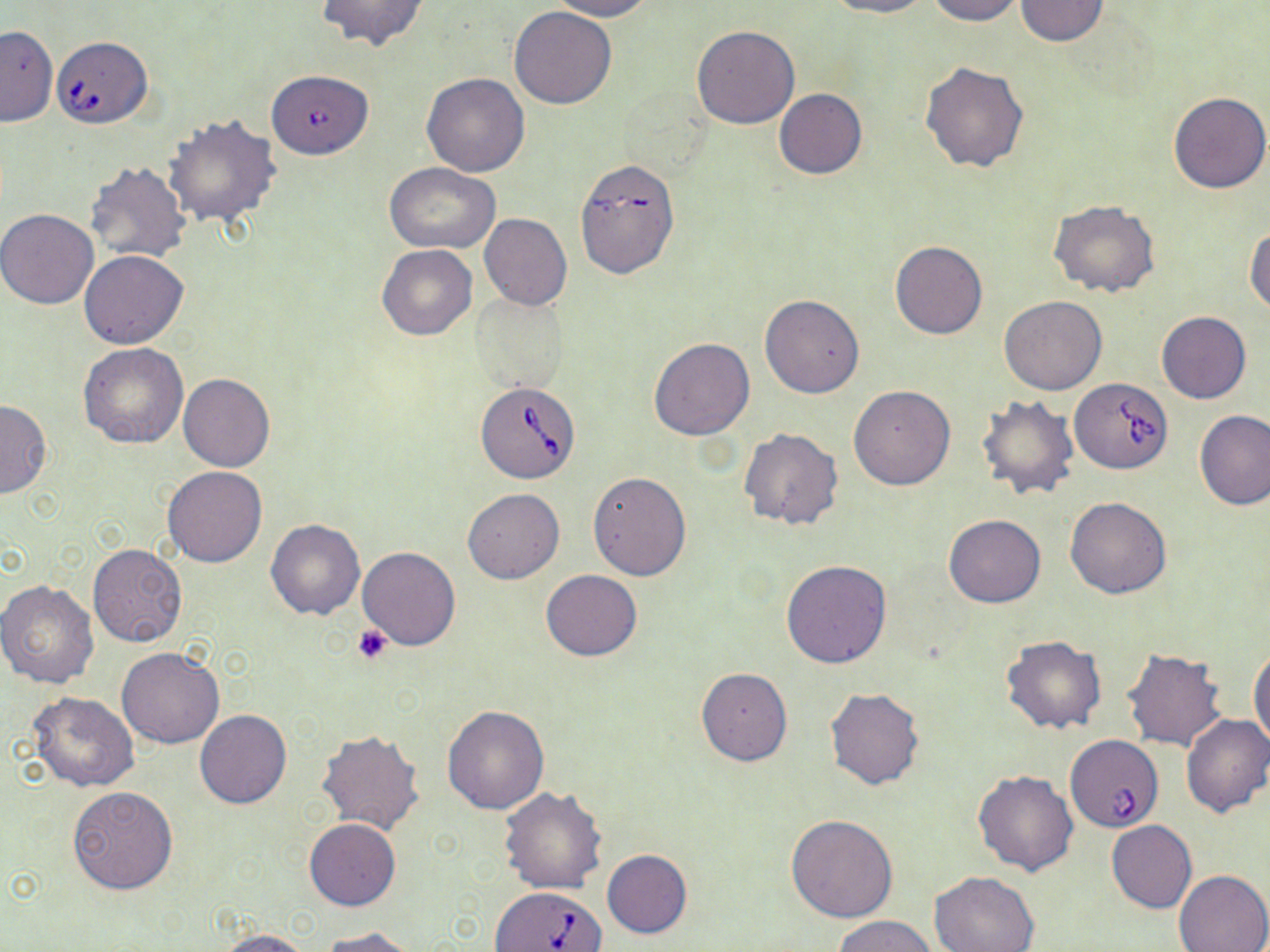
slide-level diagnosis = Babesia divergens
uninfected red blood cell locations = approximate bounding boxes as (x1, y1, x2, y2) in pixels: (317, 0, 429, 50), (547, 0, 653, 20), (826, 0, 933, 18), (925, 0, 1025, 24), (1013, 0, 1112, 46), (510, 5, 618, 108), (691, 24, 800, 128), (0, 25, 57, 127), (920, 61, 1028, 174), (421, 72, 530, 176), (773, 88, 867, 179), (1168, 92, 1269, 194), (162, 113, 281, 228), (84, 161, 190, 264), (384, 163, 500, 254), (1048, 201, 1160, 297), (0, 208, 100, 308), (479, 213, 573, 310), (1245, 223, 1270, 314), (890, 240, 987, 339), (376, 243, 478, 340), (79, 250, 188, 349), (472, 293, 567, 392), (759, 294, 865, 398), (999, 296, 1107, 395), (1156, 312, 1250, 404), (649, 337, 754, 440), (79, 342, 188, 447), (178, 373, 274, 472), (850, 386, 954, 490), (975, 394, 1080, 500), (0, 399, 51, 497), (1194, 409, 1270, 510), (737, 429, 844, 531), (163, 465, 268, 567), (588, 472, 691, 581), (463, 488, 564, 583), (1065, 496, 1172, 598), (944, 514, 1046, 607), (265, 519, 365, 620), (88, 543, 186, 647), (356, 547, 460, 651), (781, 559, 891, 668), (540, 570, 642, 660), (0, 580, 98, 688), (1002, 637, 1106, 733), (1249, 645, 1269, 752), (116, 646, 224, 748), (1121, 648, 1229, 752), (696, 669, 791, 766), (824, 687, 926, 791), (29, 692, 139, 791), (442, 705, 549, 814), (195, 710, 291, 809), (1181, 713, 1270, 818), (316, 728, 425, 835), (972, 769, 1079, 875), (67, 785, 178, 893), (499, 785, 607, 894), (786, 813, 899, 922), (304, 818, 401, 911), (1106, 820, 1196, 913), (602, 849, 692, 938), (1174, 868, 1270, 952), (929, 871, 1040, 951), (832, 915, 937, 952), (319, 927, 421, 952), (214, 928, 314, 951)
magnification = 1000x
field of view = single
Babesia divergens-infected red blood cell locations = approximate bounding boxes as (x1, y1, x2, y2) in pixels: (51, 36, 153, 128), (265, 74, 377, 164), (579, 161, 678, 284), (1069, 379, 1170, 473), (476, 381, 580, 484), (1065, 736, 1162, 833), (488, 885, 609, 952)
stain = May-Grünwald-Giemsa
preparation = thin blood smear
platelet locations = approximate bounding boxes as (x1, y1, x2, y2) in pixels: (353, 625, 393, 664)
modality = light microscopy
image size = 1270×952 pixels